Report the malaria status of this cell.
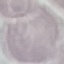

It is uninfected.

Giemsa stain. Thin smear of blood. Cell patch, automatically extracted from a larger field of view and resized to 64 × 64 pixels. Acquired by smartphone through the microscope eyepiece.